Assess this cell for malaria.
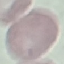

It is uninfected.

preparation = thin blood film
stain = Giemsa
capture = smartphone camera at the microscope eyepiece
image type = automatically extracted cell patch, resized to 64 × 64 pixels